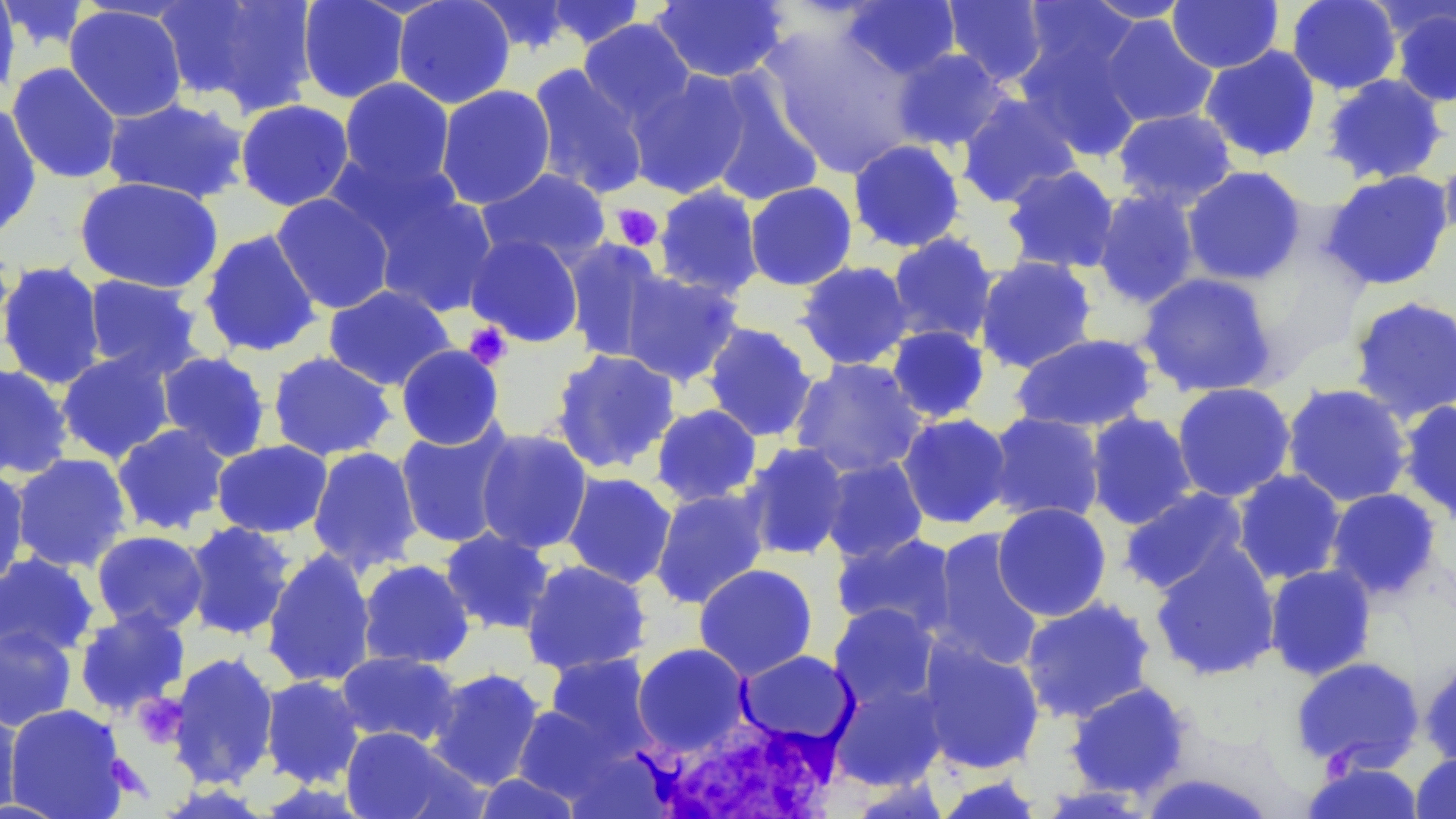
Summary:
  - Coordinate format: approximate bounding boxes as (x1, y1, x2, y2) in pixels
  - Uninfected red blood cell locations: (156, 0, 320, 116), (296, 0, 411, 104), (392, 0, 516, 109), (467, 0, 578, 55), (941, 0, 1049, 87), (1081, 0, 1193, 23), (1286, 0, 1403, 94), (1373, 0, 1456, 44), (1, 1, 93, 55), (542, 1, 648, 50), (649, 1, 790, 83), (841, 1, 961, 79), (1018, 1, 1142, 89), (1167, 1, 1284, 74), (0, 2, 21, 101), (64, 5, 188, 122), (1388, 5, 1456, 108), (1099, 15, 1218, 128), (578, 18, 696, 124), (757, 23, 926, 177), (1013, 27, 1145, 162), (1199, 45, 1322, 162), (890, 47, 1012, 153), (6, 62, 123, 184), (527, 64, 650, 200), (626, 69, 753, 200), (704, 71, 826, 207), (1320, 73, 1449, 186), (339, 77, 455, 190), (434, 84, 557, 210), (956, 92, 1082, 209), (102, 97, 251, 204), (234, 99, 355, 211), (0, 103, 42, 239), (1111, 108, 1239, 211), (848, 138, 966, 253), (1438, 145, 1456, 250), (326, 150, 466, 256), (1000, 164, 1121, 274), (1181, 165, 1307, 286), (476, 167, 611, 269), (1321, 169, 1455, 291), (74, 176, 224, 294), (743, 181, 858, 291), (653, 183, 765, 300), (364, 186, 499, 316), (1092, 189, 1202, 309), (270, 193, 396, 314), (198, 229, 323, 358), (465, 232, 585, 347), (886, 232, 998, 347), (562, 238, 669, 363), (974, 256, 1099, 374), (0, 260, 107, 390), (794, 260, 914, 370), (620, 269, 744, 387), (1137, 271, 1280, 398), (83, 274, 205, 380), (323, 284, 455, 391), (1346, 295, 1456, 424), (703, 322, 818, 442), (885, 325, 991, 424), (1009, 332, 1158, 433), (396, 344, 505, 450), (548, 348, 681, 475), (56, 349, 177, 464), (156, 350, 272, 462), (267, 351, 397, 461), (789, 357, 927, 479), (0, 363, 74, 480), (1171, 382, 1297, 503), (1281, 383, 1413, 507), (1396, 399, 1456, 525), (650, 403, 762, 507), (1084, 411, 1197, 530), (896, 412, 1013, 530), (984, 412, 1106, 525), (393, 422, 516, 549), (111, 423, 232, 536), (474, 428, 593, 555), (211, 439, 333, 538), (740, 442, 852, 561), (307, 446, 423, 576), (9, 453, 132, 573), (819, 455, 928, 564), (0, 465, 31, 592), (1231, 468, 1347, 586), (561, 471, 678, 589), (649, 487, 770, 609), (1118, 487, 1251, 597), (1325, 488, 1443, 603), (991, 502, 1112, 621), (182, 521, 296, 640), (439, 527, 557, 636), (928, 528, 1046, 673), (91, 530, 209, 634), (830, 531, 960, 639), (1149, 543, 1281, 681), (262, 548, 377, 688), (0, 552, 100, 660), (357, 559, 475, 669), (520, 559, 652, 676), (693, 563, 818, 680), (1264, 564, 1377, 681), (1019, 596, 1157, 723), (827, 602, 942, 713), (73, 607, 191, 717), (0, 625, 78, 732), (916, 636, 1046, 775), (632, 642, 752, 754), (736, 650, 858, 747), (167, 651, 280, 790), (334, 651, 463, 748), (543, 653, 657, 759), (1289, 656, 1425, 773), (1418, 656, 1456, 769), (425, 667, 546, 790), (259, 675, 365, 788), (829, 677, 949, 791), (1064, 681, 1195, 801), (0, 698, 23, 817), (5, 704, 128, 818), (511, 704, 624, 805), (339, 726, 473, 819), (1410, 752, 1456, 818), (1300, 759, 1424, 819), (1136, 771, 1279, 818), (471, 772, 583, 818), (931, 774, 1047, 818)
  - White blood cell locations: (636, 711, 850, 818)
  - Platelet locations: (611, 204, 664, 251), (463, 322, 512, 369), (133, 692, 189, 749), (106, 754, 149, 799)
  - Slide-level diagnosis: no evidence of blood parasites
  - Stain: May-Grünwald-Giemsa
  - Magnification: 1000x
  - Preparation: thin blood smear
  - Modality: optical microscopy
  - Image size: 1456×819 pixels
  - Field of view: single